State the blood parasite species.
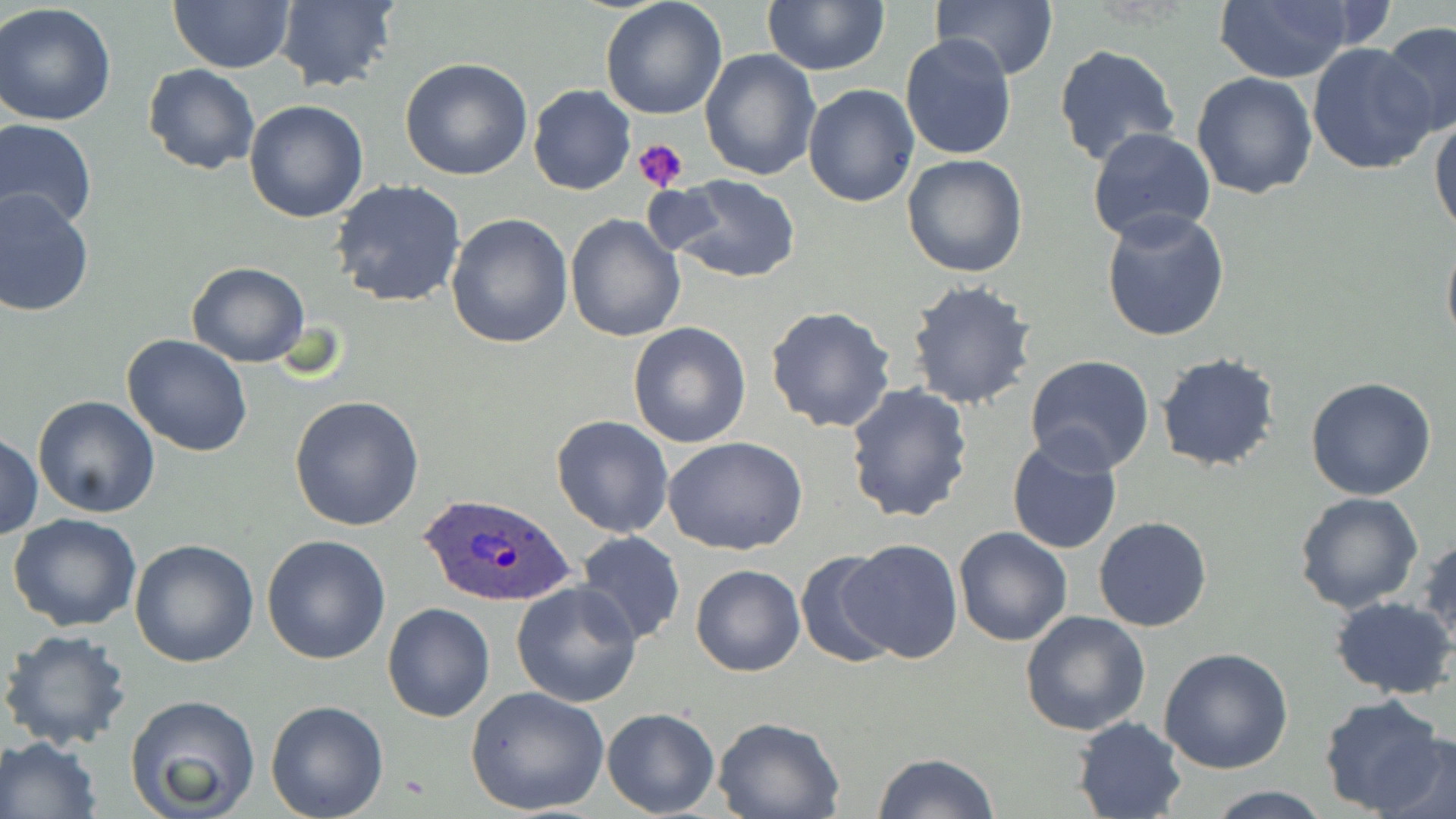
Plasmodium ovale.

modality = light microscopy
Plasmodium ovale-infected red blood cell locations = approximate bounding boxes as named x1/y1/x2/y2 corners in pixels: (x1=417, y1=490, x2=574, y2=608)
uninfected red blood cell locations = approximate bounding boxes as named x1/y1/x2/y2 corners in pixels: (x1=600, y1=0, x2=728, y2=119), (x1=932, y1=0, x2=1056, y2=81), (x1=169, y1=1, x2=294, y2=73), (x1=272, y1=1, x2=400, y2=92), (x1=762, y1=1, x2=889, y2=75), (x1=1212, y1=2, x2=1358, y2=83), (x1=0, y1=3, x2=117, y2=127), (x1=1378, y1=21, x2=1456, y2=136), (x1=900, y1=34, x2=1017, y2=158), (x1=1307, y1=43, x2=1439, y2=175), (x1=1052, y1=44, x2=1181, y2=167), (x1=699, y1=47, x2=820, y2=180), (x1=399, y1=57, x2=533, y2=181), (x1=142, y1=64, x2=260, y2=174), (x1=1191, y1=72, x2=1318, y2=199), (x1=803, y1=82, x2=919, y2=206), (x1=528, y1=85, x2=635, y2=196), (x1=243, y1=99, x2=367, y2=222), (x1=1430, y1=115, x2=1456, y2=237), (x1=1, y1=118, x2=98, y2=234), (x1=1086, y1=129, x2=1216, y2=245), (x1=902, y1=154, x2=1030, y2=278), (x1=665, y1=173, x2=802, y2=283), (x1=330, y1=180, x2=467, y2=308), (x1=0, y1=189, x2=96, y2=317), (x1=1099, y1=206, x2=1230, y2=342), (x1=445, y1=213, x2=574, y2=349), (x1=566, y1=215, x2=685, y2=340), (x1=1441, y1=235, x2=1456, y2=352), (x1=186, y1=262, x2=310, y2=366), (x1=904, y1=280, x2=1037, y2=410), (x1=766, y1=305, x2=896, y2=433), (x1=627, y1=322, x2=751, y2=449), (x1=121, y1=335, x2=253, y2=458), (x1=1155, y1=352, x2=1283, y2=472), (x1=1023, y1=357, x2=1155, y2=476), (x1=1305, y1=375, x2=1437, y2=501), (x1=844, y1=382, x2=974, y2=525), (x1=32, y1=394, x2=161, y2=518), (x1=289, y1=394, x2=424, y2=531), (x1=550, y1=414, x2=675, y2=538), (x1=1, y1=432, x2=43, y2=541), (x1=664, y1=437, x2=810, y2=554), (x1=1007, y1=437, x2=1123, y2=556), (x1=1293, y1=491, x2=1423, y2=612), (x1=7, y1=512, x2=142, y2=633), (x1=1094, y1=516, x2=1213, y2=633), (x1=953, y1=526, x2=1071, y2=647), (x1=575, y1=531, x2=686, y2=645), (x1=1417, y1=531, x2=1456, y2=650), (x1=261, y1=534, x2=391, y2=665), (x1=129, y1=539, x2=258, y2=667), (x1=837, y1=539, x2=964, y2=662), (x1=794, y1=549, x2=902, y2=667), (x1=691, y1=565, x2=806, y2=677), (x1=511, y1=581, x2=642, y2=706), (x1=1331, y1=596, x2=1456, y2=699), (x1=380, y1=602, x2=495, y2=723), (x1=1019, y1=611, x2=1152, y2=735), (x1=0, y1=629, x2=133, y2=752), (x1=1159, y1=647, x2=1295, y2=774), (x1=464, y1=685, x2=609, y2=816), (x1=1318, y1=693, x2=1450, y2=817), (x1=126, y1=694, x2=261, y2=819), (x1=265, y1=699, x2=389, y2=819), (x1=601, y1=707, x2=720, y2=817), (x1=1072, y1=716, x2=1185, y2=819), (x1=714, y1=717, x2=843, y2=819), (x1=1372, y1=732, x2=1455, y2=819), (x1=0, y1=735, x2=103, y2=818), (x1=871, y1=752, x2=1003, y2=819), (x1=1203, y1=785, x2=1333, y2=818)
magnification = 1000x
platelet locations = approximate bounding boxes as named x1/y1/x2/y2 corners in pixels: (x1=632, y1=136, x2=689, y2=191)
preparation = thin blood smear
image size = 1456×819 pixels
field of view = single
stain = May-Grünwald-Giemsa